Point out each Plasmodium parasite.
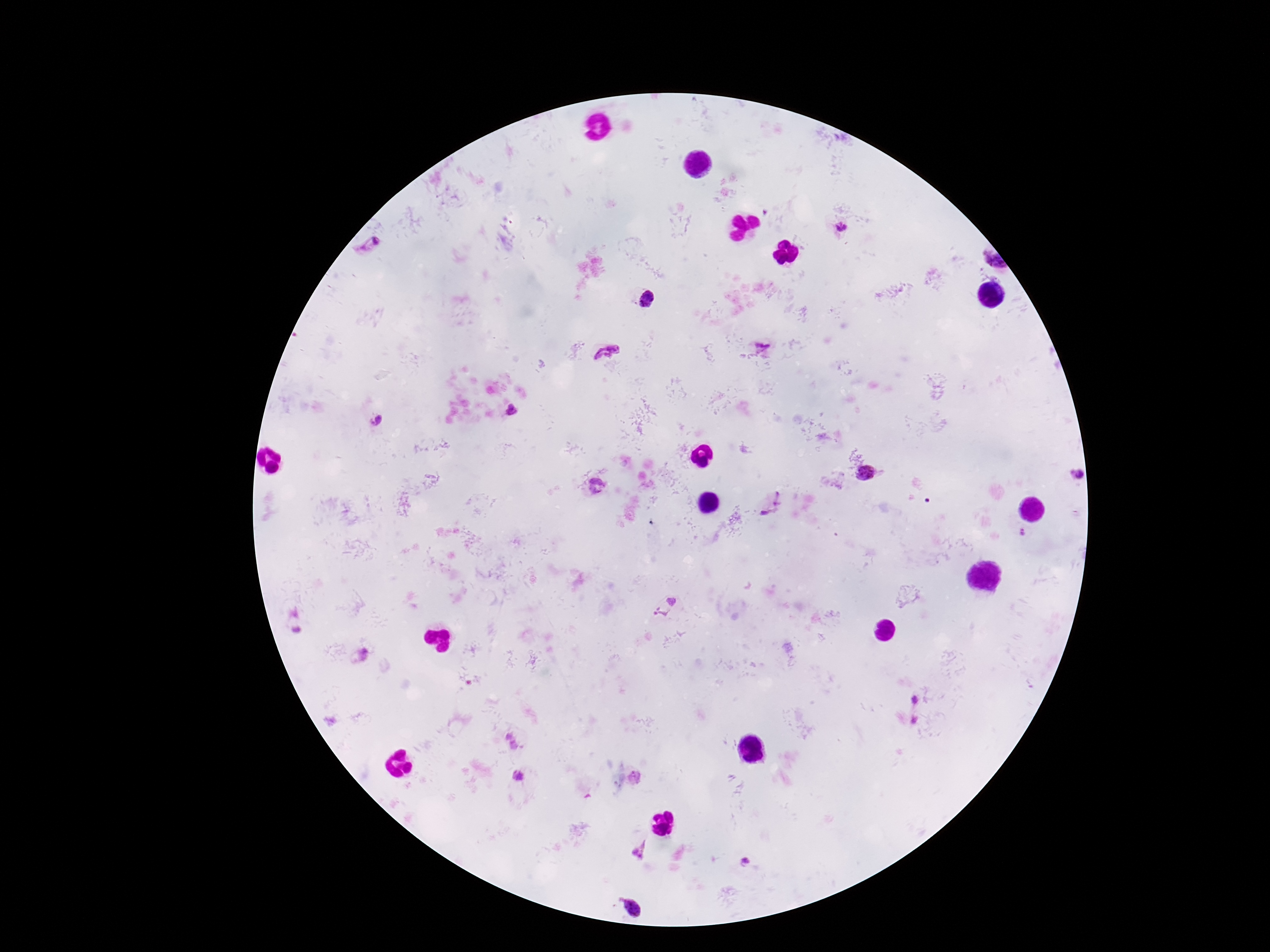
Approximate centers as [x, y] in pixels.
Plasmodium parasites: [841, 229], [369, 249], [993, 262], [647, 300], [761, 344], [607, 353], [511, 410], [378, 421], [866, 473], [1075, 473], [598, 487], [771, 505], [666, 606], [360, 656], [916, 700], [915, 720], [512, 741], [519, 777], [634, 778], [642, 850], [745, 863], [631, 906].

{
  "stain": "Giemsa",
  "image_size": "1270×952 pixels",
  "patient_malaria_status": "infected",
  "preparation": "thick blood film",
  "capture": "smartphone camera through the microscope eyepiece",
  "field_of_view": "single",
  "magnification": "100x"
}